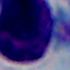

magnification: 1000x
identification: white blood cell
modality: micrograph